Name the blood parasite species.
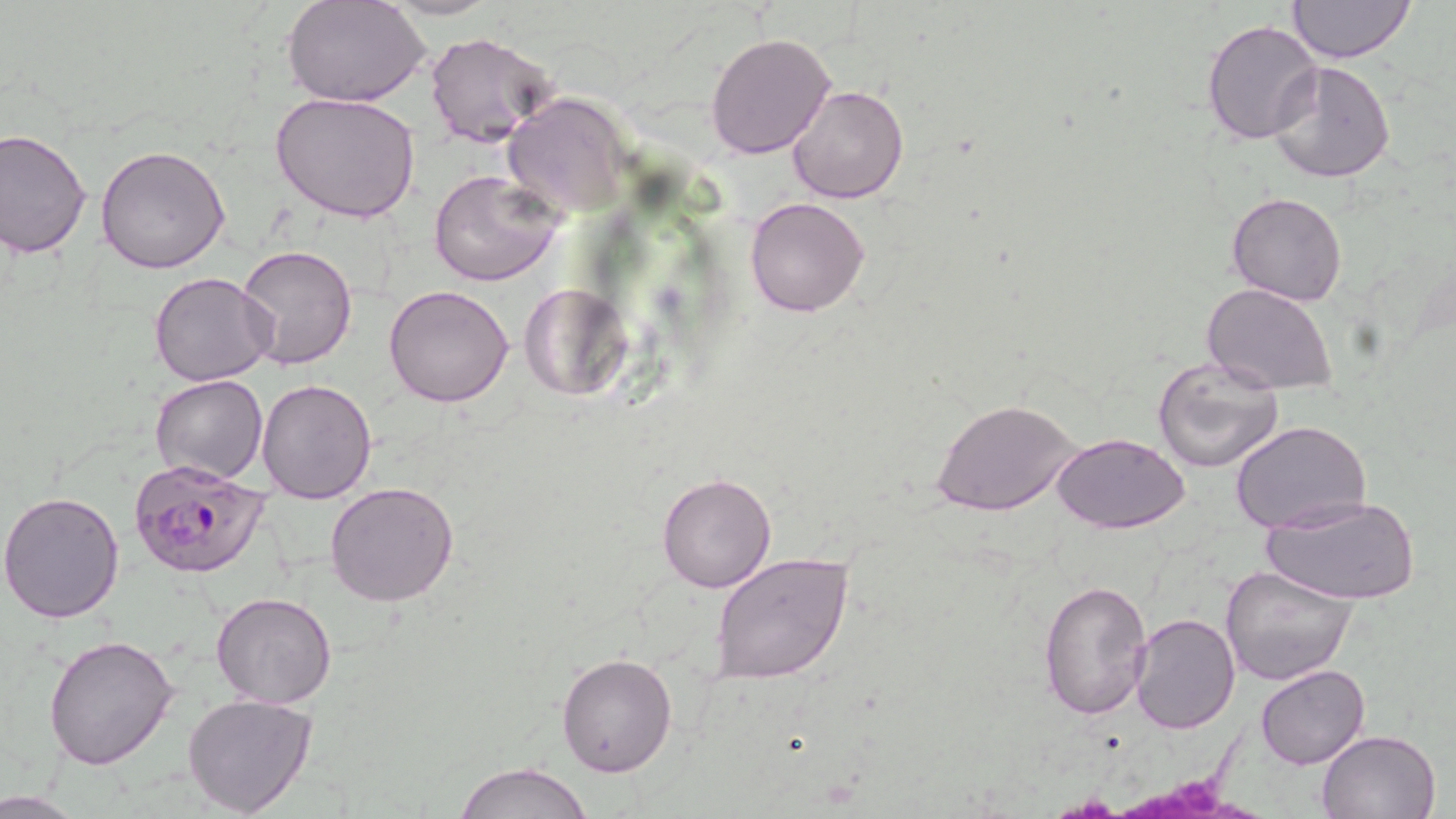
Plasmodium falciparum.

image size = 1456×819 pixels
Plasmodium falciparum-infected red blood cell locations = approximate bounding boxes as (x1, y1, x2, y2) in pixels: (128, 457, 270, 579)
field of view = single
stain = May-Grünwald-Giemsa
preparation = thin blood smear
uninfected red blood cell locations = approximate bounding boxes as (x1, y1, x2, y2) in pixels: (284, 0, 430, 108), (380, 0, 503, 20), (1286, 0, 1417, 65), (1202, 19, 1323, 145), (425, 30, 559, 151), (706, 31, 836, 158), (1268, 61, 1395, 184), (787, 86, 908, 203), (270, 91, 421, 223), (501, 93, 630, 218), (0, 128, 92, 257), (95, 144, 231, 273), (429, 169, 565, 286), (1226, 191, 1349, 306), (745, 196, 870, 316), (237, 243, 360, 371), (149, 272, 276, 387), (516, 282, 631, 401), (383, 284, 514, 408), (1202, 284, 1339, 396), (1153, 355, 1286, 475), (150, 374, 269, 485), (257, 378, 377, 504), (933, 399, 1082, 517), (1231, 420, 1372, 533), (1050, 432, 1191, 534), (656, 471, 777, 593), (326, 481, 459, 606), (0, 491, 126, 624), (1263, 492, 1419, 607), (710, 552, 854, 685), (1219, 564, 1360, 686), (1037, 578, 1152, 721), (211, 592, 338, 709), (1129, 612, 1242, 733), (43, 634, 179, 771), (554, 652, 677, 776), (1255, 663, 1369, 769), (181, 693, 317, 817), (1315, 730, 1442, 819), (454, 761, 594, 819), (0, 790, 91, 818)
magnification = 1000x
modality = light microscopy